Point out each leukocyte.
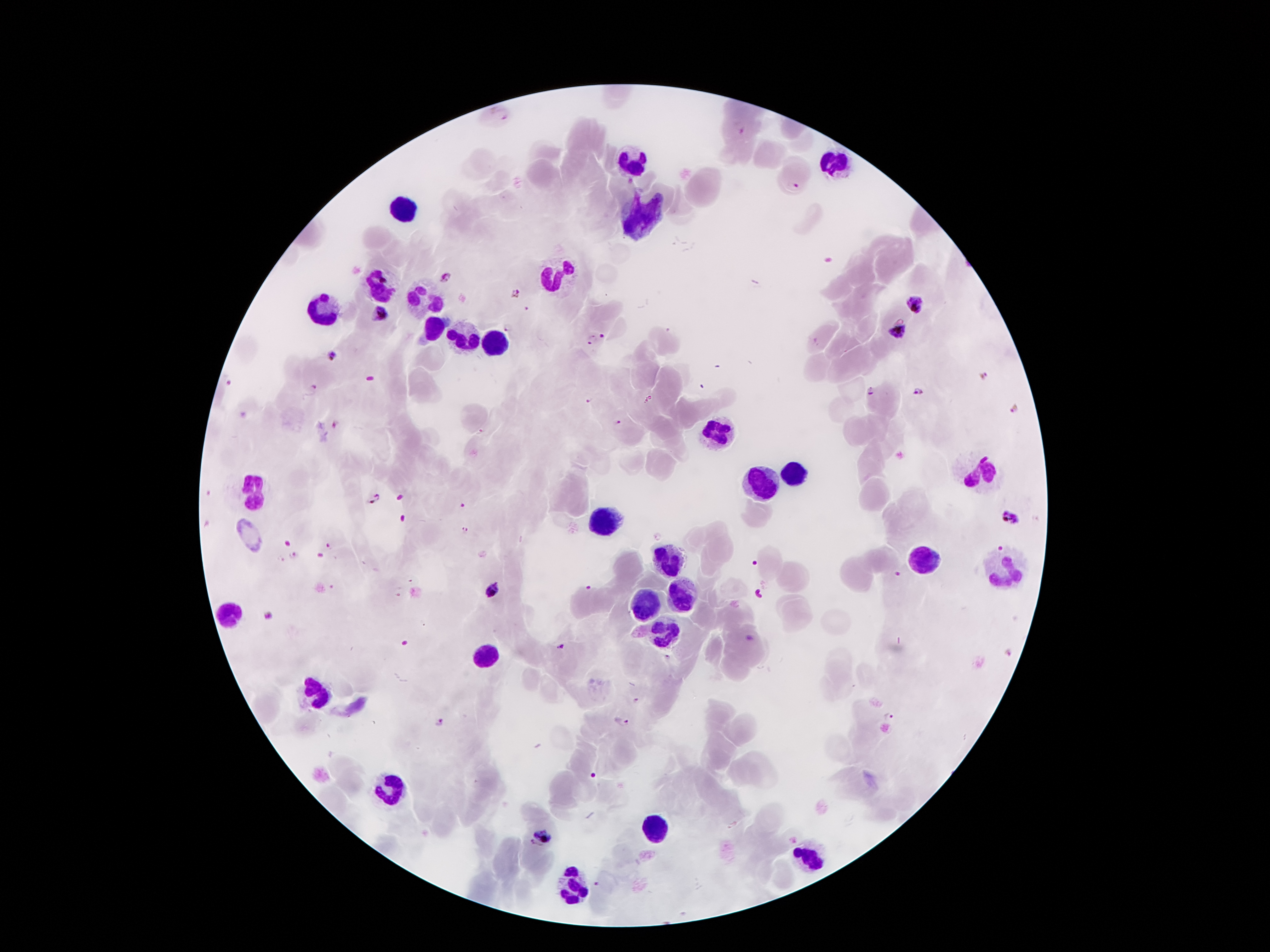

Approximate object centers, in pixels from the top-left corner.
Leukocytes: (x=633, y=160), (x=832, y=160), (x=402, y=210), (x=641, y=215), (x=554, y=274), (x=376, y=285), (x=427, y=303), (x=323, y=308), (x=433, y=331), (x=466, y=338), (x=491, y=340), (x=718, y=432), (x=988, y=468), (x=792, y=475), (x=764, y=481), (x=252, y=488), (x=605, y=521), (x=927, y=552), (x=667, y=560), (x=1003, y=570), (x=682, y=592), (x=646, y=602), (x=234, y=608), (x=667, y=633), (x=483, y=656), (x=318, y=694), (x=390, y=789), (x=654, y=830), (x=807, y=858), (x=573, y=886).

Malaria parasite locations: (x=502, y=112), (x=742, y=127), (x=793, y=184), (x=445, y=276), (x=516, y=292), (x=917, y=303), (x=377, y=312), (x=507, y=326), (x=899, y=333), (x=604, y=336), (x=591, y=340), (x=330, y=354), (x=983, y=376), (x=312, y=390), (x=869, y=392), (x=917, y=392), (x=589, y=400), (x=1015, y=410), (x=616, y=423), (x=338, y=424), (x=374, y=496), (x=1008, y=516), (x=465, y=530), (x=330, y=547), (x=293, y=556), (x=491, y=590), (x=269, y=615), (x=559, y=647), (x=890, y=715), (x=438, y=722), (x=622, y=722), (x=543, y=833), (x=535, y=846), (x=596, y=884). Single field of view. Giemsa stain. 100x magnification. Patient malaria status: infected with Plasmodium falciparum. Photographed through the microscope eyepiece with a smartphone camera. Image is 1270×952 pixels. Thick blood smear.